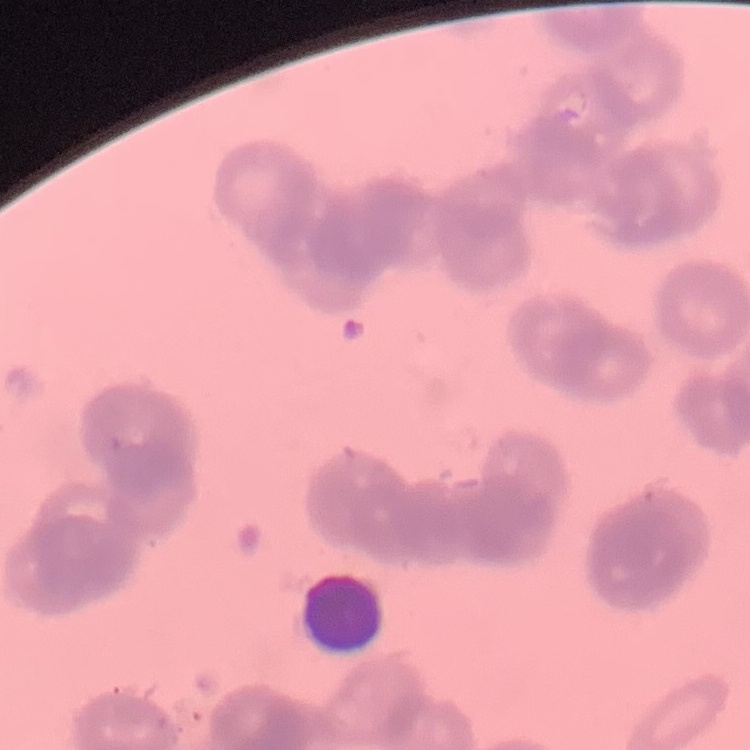

Summary:
  - Red blood cell morphology: rouleaux formation
  - Stain: Field's or Giemsa
  - Preparation: thin blood film
  - Image type: square crop of a larger photomicrograph